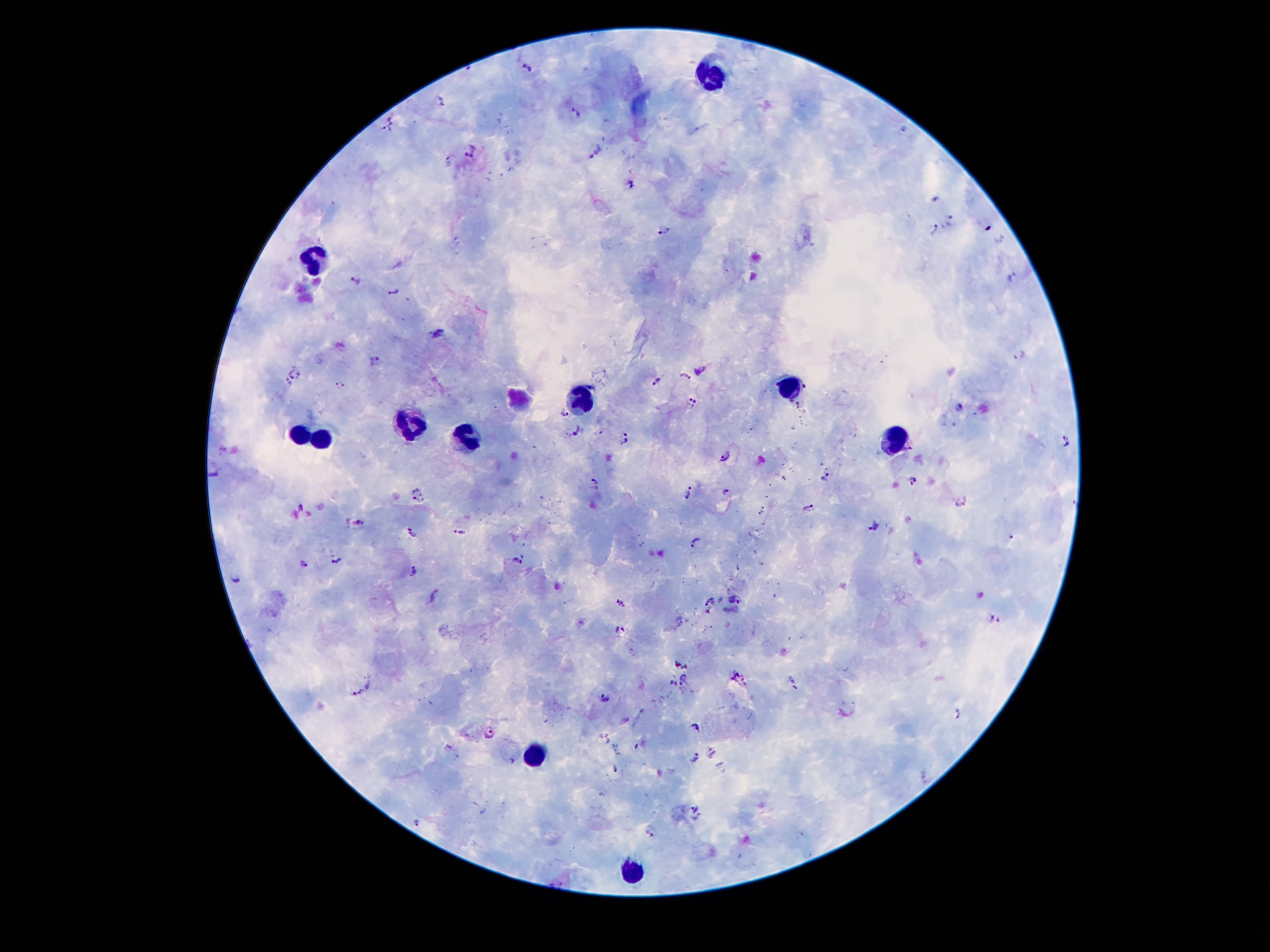

{
  "stain": "Giemsa",
  "magnification": "100x",
  "preparation": "thick blood film",
  "leukocyte_locations": "approximate object centers, in pixels from the top-left corner: (x=711, y=76), (x=314, y=262), (x=791, y=382), (x=580, y=395), (x=407, y=414), (x=298, y=432), (x=323, y=432), (x=895, y=435), (x=466, y=439), (x=532, y=753), (x=630, y=872)",
  "patient_malaria_status": "infected with Plasmodium falciparum",
  "capture": "smartphone camera through the microscope eyepiece",
  "image_size": "1270×952 pixels",
  "malaria_parasite_locations": "approximate object centers, in pixels from the top-left corner: (x=526, y=65), (x=440, y=98), (x=574, y=112), (x=391, y=120), (x=470, y=149), (x=596, y=149), (x=633, y=185), (x=936, y=200), (x=951, y=220), (x=664, y=228), (x=934, y=230), (x=1011, y=275), (x=358, y=278), (x=393, y=292), (x=437, y=332), (x=1020, y=354), (x=375, y=358), (x=699, y=373), (x=297, y=375), (x=685, y=375), (x=290, y=379), (x=656, y=379), (x=339, y=384), (x=805, y=386), (x=693, y=404), (x=799, y=404), (x=958, y=406), (x=564, y=413), (x=573, y=433), (x=624, y=437), (x=1065, y=440), (x=724, y=454), (x=211, y=468), (x=826, y=477), (x=915, y=478), (x=594, y=482), (x=690, y=491), (x=724, y=493), (x=415, y=494), (x=423, y=501), (x=960, y=503), (x=300, y=504), (x=808, y=508), (x=358, y=524), (x=874, y=527), (x=459, y=531), (x=412, y=534), (x=694, y=541), (x=334, y=559), (x=517, y=560), (x=304, y=566), (x=412, y=569), (x=236, y=578), (x=433, y=595), (x=735, y=599), (x=710, y=601), (x=621, y=605), (x=993, y=618), (x=623, y=630), (x=677, y=664), (x=687, y=668), (x=736, y=676), (x=683, y=679), (x=791, y=680), (x=670, y=682), (x=356, y=691), (x=605, y=696), (x=959, y=713), (x=697, y=726), (x=491, y=732), (x=606, y=739), (x=637, y=748), (x=711, y=753), (x=694, y=757), (x=614, y=769), (x=694, y=807), (x=418, y=821), (x=650, y=831)",
  "field_of_view": "one from this slide"
}